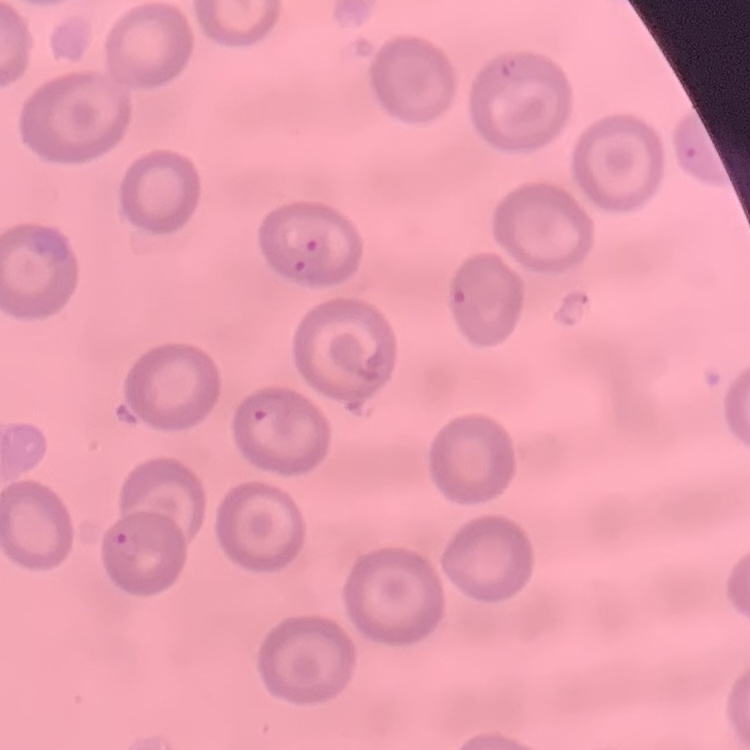

Summary:
  - Red blood cell morphology: no rouleaux formation
  - Preparation: thin blood film
  - Stain: Field's or Giemsa
  - Image type: one tile cut from a larger photomicrograph